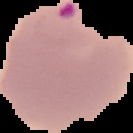

Summary:
  - Image type: cell region segmented out of the field of view; surrounding area masked to black
  - Preparation: thin blood smear
  - Image size: 133×133 pixels
  - Malaria status: parasitized